Report the malaria status of this cell.
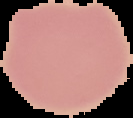
Uninfected.

{
  "image_type": "segmented cell region with the area outside set to black",
  "preparation": "thin blood film",
  "image_size": "133×118 pixels"
}